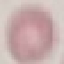
result = no malaria parasites seen
preparation = thin smear
capture = smartphone through the microscope eyepiece
stain = Giemsa
image type = automatically extracted cell patch, resized to 64 × 64 pixels